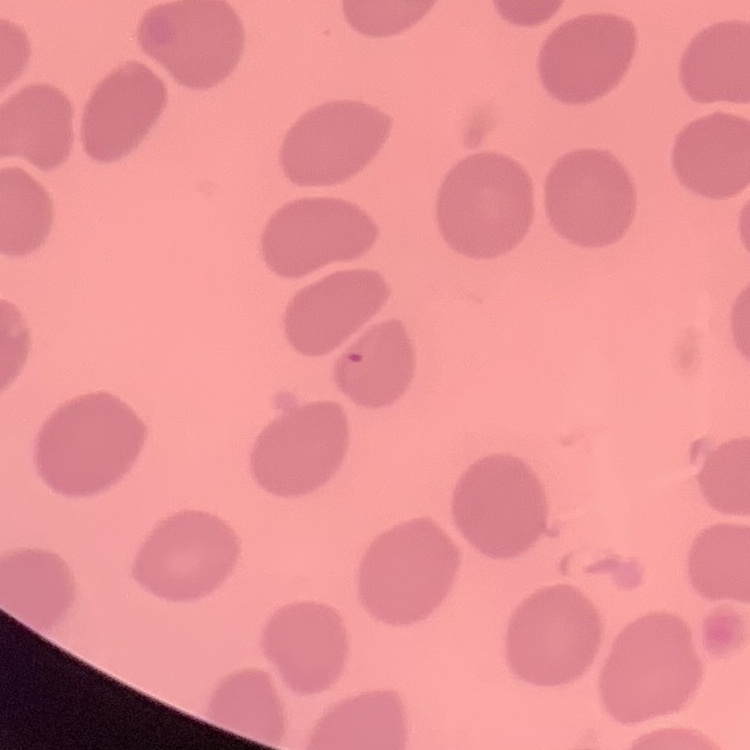 The red blood cells show no rouleaux formation. Square crop of a larger photomicrograph. Stained with either Field's or Giemsa. Thin blood smear.